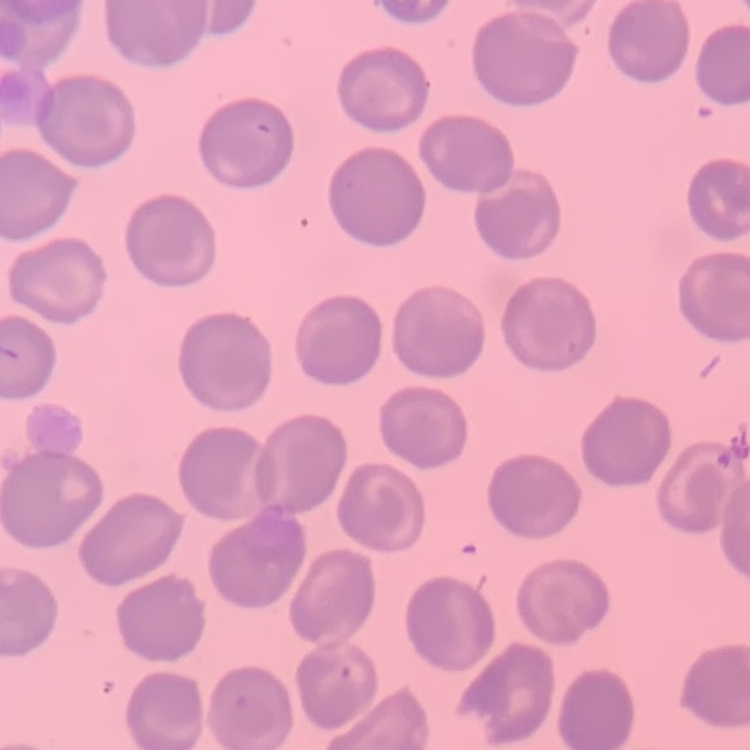
Summary:
  - Erythrocyte morphology: no rouleaux formation
  - Image type: square crop of a larger photomicrograph
  - Stain: Field's or Giemsa
  - Preparation: thin peripheral smear